Point out each Plasmodium parasite.
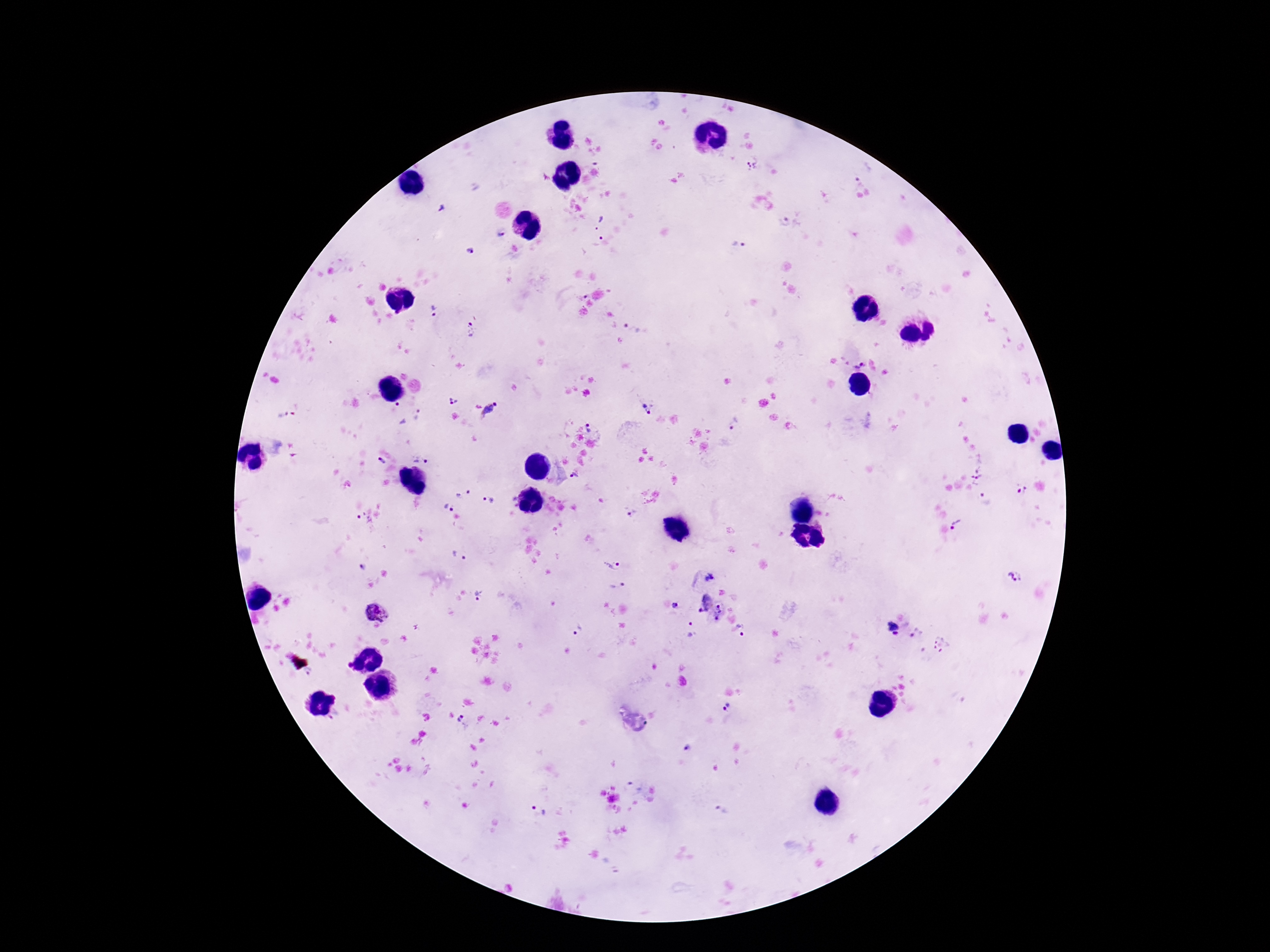
Approximate centers as {x, y} in pixels.
Plasmodium parasites: {751, 166}, {862, 180}, {443, 208}, {783, 220}, {599, 223}, {498, 234}, {595, 239}, {739, 246}, {471, 252}, {434, 311}, {632, 326}, {470, 329}, {860, 363}, {453, 402}, {646, 408}, {492, 411}, {396, 413}, {282, 416}, {420, 416}, {735, 423}, {592, 427}, {421, 456}, {380, 460}, {976, 474}, {574, 477}, {1022, 490}, {464, 493}, {985, 498}, {488, 500}, {448, 508}, {631, 515}, {363, 520}, {958, 524}, {460, 556}, {609, 564}, {363, 568}, {711, 577}, {1016, 577}, {613, 585}, {481, 595}, {703, 603}, {677, 607}, {376, 610}, {720, 613}, {576, 628}, {690, 628}, {893, 629}, {743, 631}, {915, 632}, {941, 646}, {308, 674}, {726, 707}, {464, 721}, {686, 748}, {539, 810}, {722, 812}.

Thick blood smear. Giemsa stain. 100x magnification. Patient malaria status: positive. Image is 1270×952 pixels. Photographed through the microscope eyepiece with a smartphone camera. One field from this slide.